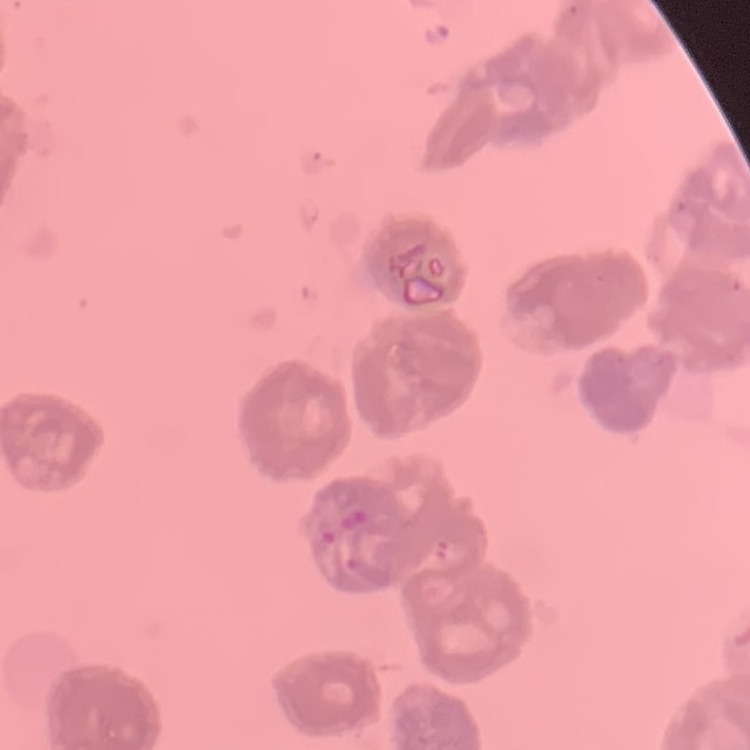
red_blood_cell_morphology: rouleaux formation
image_type: one tile cut from a larger photomicrograph
stain: Field's or Giemsa
preparation: thin blood film